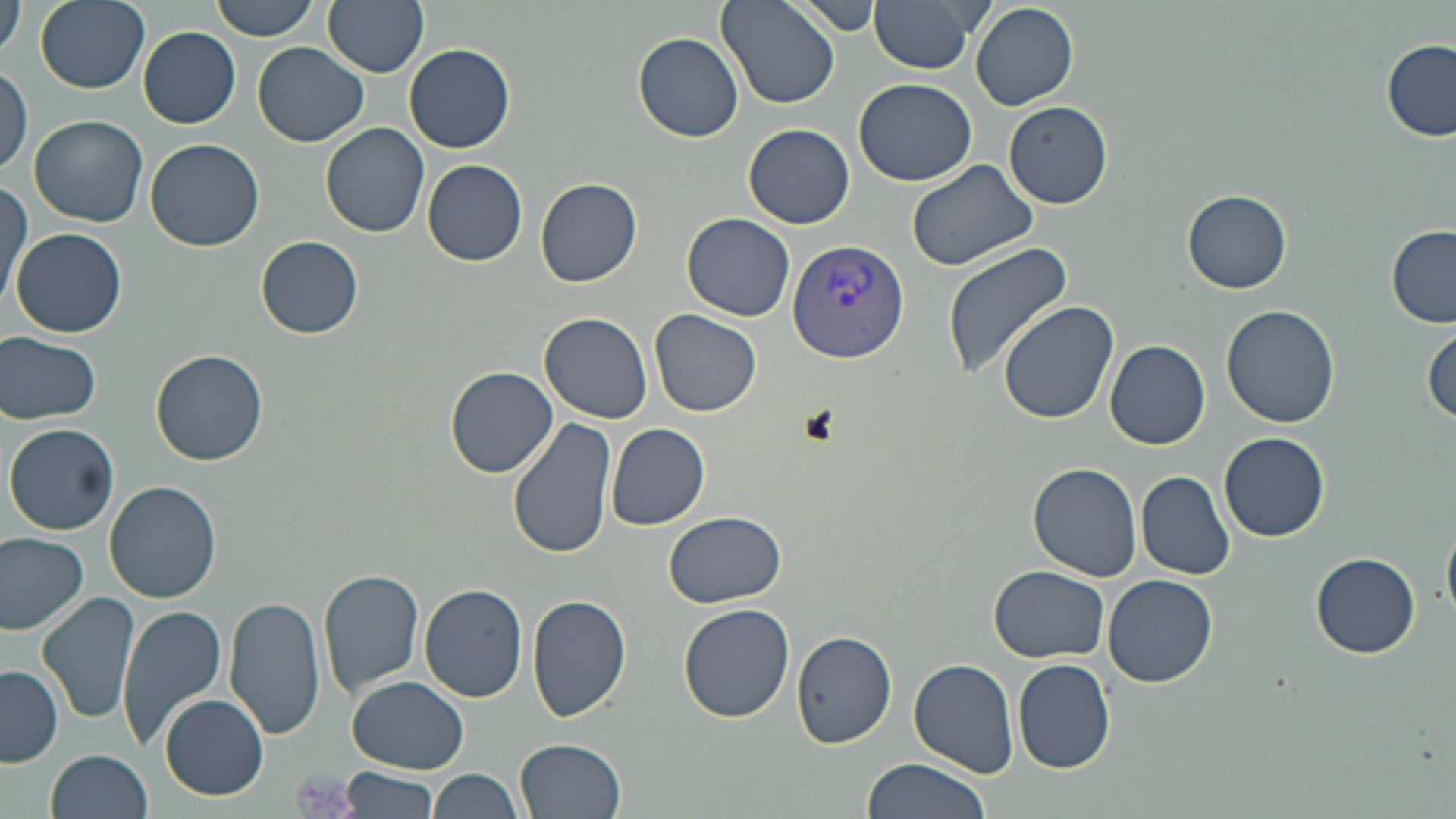

slide-level diagnosis = Plasmodium vivax
preparation = thin blood film
uninfected red blood cell locations = approximate bounding boxes as named x1/y1/x2/y2 corners in pixels: (x1=0, y1=0, x2=27, y2=59), (x1=36, y1=0, x2=150, y2=93), (x1=210, y1=0, x2=322, y2=41), (x1=323, y1=0, x2=429, y2=76), (x1=716, y1=0, x2=839, y2=110), (x1=791, y1=0, x2=882, y2=34), (x1=868, y1=0, x2=987, y2=74), (x1=970, y1=3, x2=1077, y2=111), (x1=138, y1=26, x2=241, y2=128), (x1=634, y1=33, x2=743, y2=142), (x1=1380, y1=39, x2=1456, y2=141), (x1=253, y1=41, x2=370, y2=147), (x1=405, y1=43, x2=515, y2=153), (x1=0, y1=66, x2=31, y2=178), (x1=853, y1=77, x2=979, y2=185), (x1=1004, y1=101, x2=1113, y2=208), (x1=29, y1=113, x2=148, y2=227), (x1=321, y1=121, x2=430, y2=236), (x1=744, y1=124, x2=854, y2=230), (x1=146, y1=139, x2=264, y2=251), (x1=905, y1=157, x2=1043, y2=273), (x1=422, y1=159, x2=528, y2=267), (x1=535, y1=178, x2=642, y2=287), (x1=1, y1=180, x2=31, y2=310), (x1=1183, y1=188, x2=1291, y2=294), (x1=682, y1=213, x2=795, y2=321), (x1=1385, y1=224, x2=1456, y2=327), (x1=11, y1=227, x2=128, y2=338), (x1=256, y1=236, x2=364, y2=339), (x1=943, y1=242, x2=1075, y2=379), (x1=997, y1=301, x2=1121, y2=424), (x1=1221, y1=304, x2=1340, y2=427), (x1=650, y1=310, x2=762, y2=417), (x1=539, y1=312, x2=653, y2=424), (x1=1425, y1=325, x2=1456, y2=429), (x1=2, y1=331, x2=104, y2=423), (x1=1106, y1=339, x2=1210, y2=451), (x1=152, y1=350, x2=268, y2=464), (x1=446, y1=367, x2=556, y2=477), (x1=508, y1=415, x2=613, y2=560), (x1=5, y1=422, x2=120, y2=534), (x1=605, y1=423, x2=711, y2=530), (x1=1219, y1=432, x2=1331, y2=541), (x1=1028, y1=461, x2=1143, y2=581), (x1=1136, y1=469, x2=1235, y2=580), (x1=105, y1=480, x2=223, y2=603), (x1=663, y1=510, x2=788, y2=608), (x1=1443, y1=516, x2=1456, y2=624), (x1=668, y1=527, x2=789, y2=691), (x1=0, y1=530, x2=91, y2=636), (x1=1312, y1=552, x2=1420, y2=657), (x1=989, y1=567, x2=1110, y2=663), (x1=319, y1=569, x2=424, y2=697), (x1=1103, y1=574, x2=1217, y2=686), (x1=419, y1=582, x2=529, y2=701), (x1=39, y1=591, x2=138, y2=726), (x1=526, y1=593, x2=631, y2=721), (x1=225, y1=597, x2=326, y2=740), (x1=677, y1=603, x2=794, y2=723), (x1=118, y1=605, x2=228, y2=747), (x1=791, y1=627, x2=898, y2=750), (x1=1012, y1=656, x2=1115, y2=774), (x1=908, y1=658, x2=1019, y2=776), (x1=0, y1=665, x2=62, y2=767), (x1=348, y1=677, x2=468, y2=772), (x1=160, y1=693, x2=268, y2=800), (x1=517, y1=737, x2=626, y2=818), (x1=45, y1=749, x2=153, y2=819), (x1=860, y1=758, x2=989, y2=819), (x1=341, y1=767, x2=439, y2=818), (x1=429, y1=770, x2=524, y2=819)
image size = 1456×819 pixels
stain = May-Grünwald-Giemsa
Plasmodium vivax-infected red blood cell locations = approximate bounding boxes as named x1/y1/x2/y2 corners in pixels: (x1=788, y1=240, x2=910, y2=363)
platelet locations = approximate bounding boxes as named x1/y1/x2/y2 corners in pixels: (x1=290, y1=767, x2=358, y2=819)
magnification = 1000x
modality = optical microscopy
field of view = one of a larger specimen